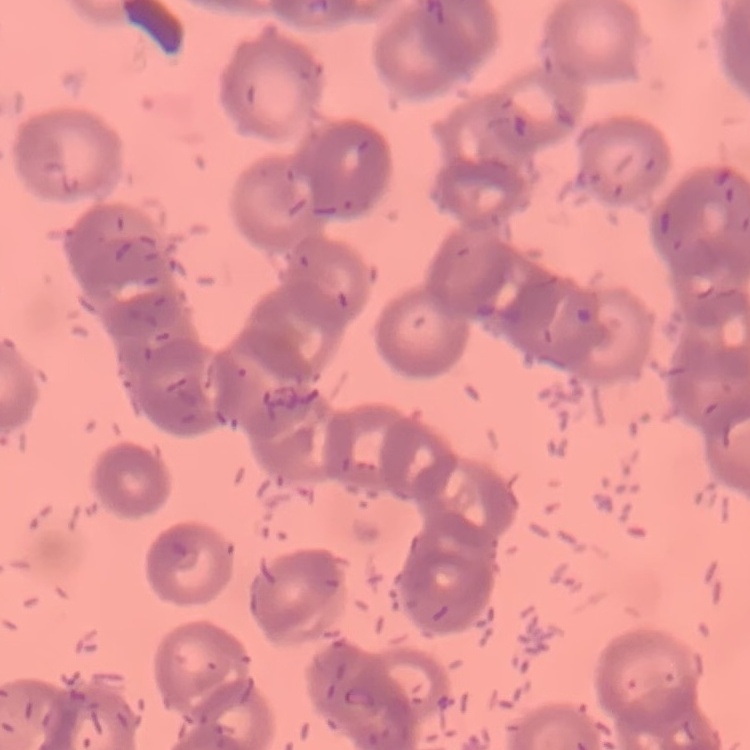

The red blood cells exhibit rouleaux formation. Square crop of a larger photomicrograph. Field's or Giemsa stain. Thin blood film.